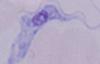
magnification = 1000x
identification = trypanosome
modality = micrograph